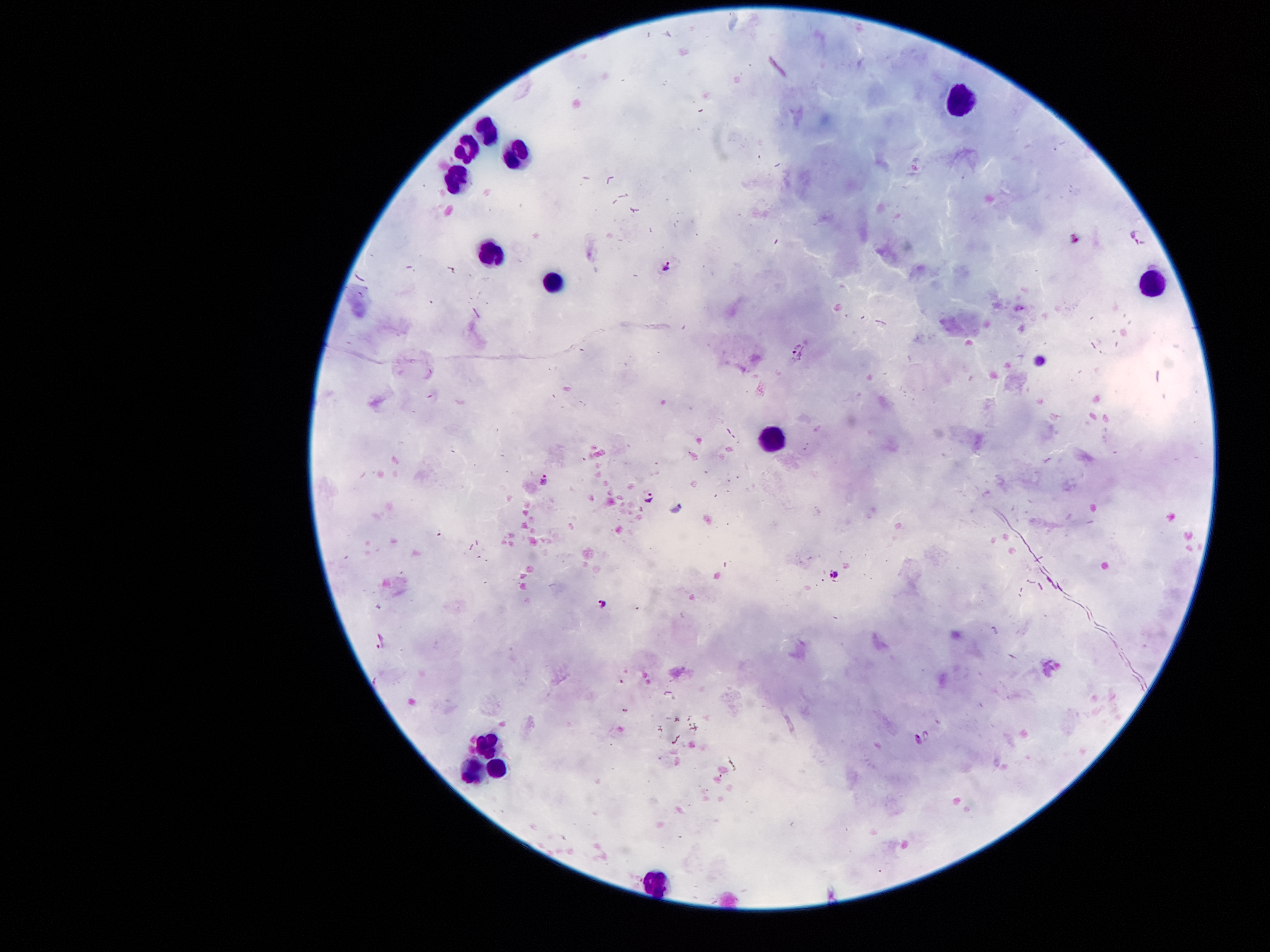
coordinate format = approximate centers as [x, y] in pixels
Plasmodium parasite locations = [1141, 236], [665, 266], [796, 351], [544, 480], [648, 495], [676, 508], [839, 576], [602, 602], [380, 639], [917, 739]
leukocyte locations = [956, 99], [484, 132], [464, 147], [518, 152], [458, 180], [490, 253], [553, 282], [1152, 285], [772, 437], [486, 744], [499, 769], [473, 771], [652, 881]
patient malaria status = infected with Plasmodium falciparum
preparation = thick peripheral-blood smear
magnification = 100x
stain = Giemsa
image size = 1270×952 pixels
capture = smartphone camera through the microscope eyepiece
field of view = single